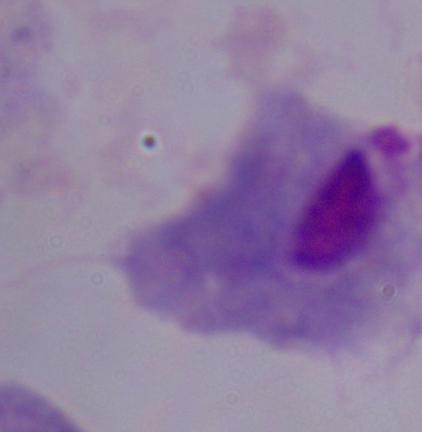

modality: micrograph
magnification: 1000x
identification: trichomonad